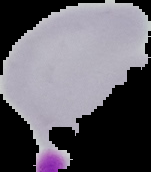

preparation = thin blood film
image type = segmented cell region on a black background
malaria status = uninfected
image size = 151×172 pixels